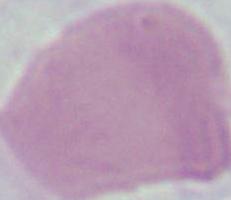

A red blood cell is shown. Micrograph. 1000x magnification.